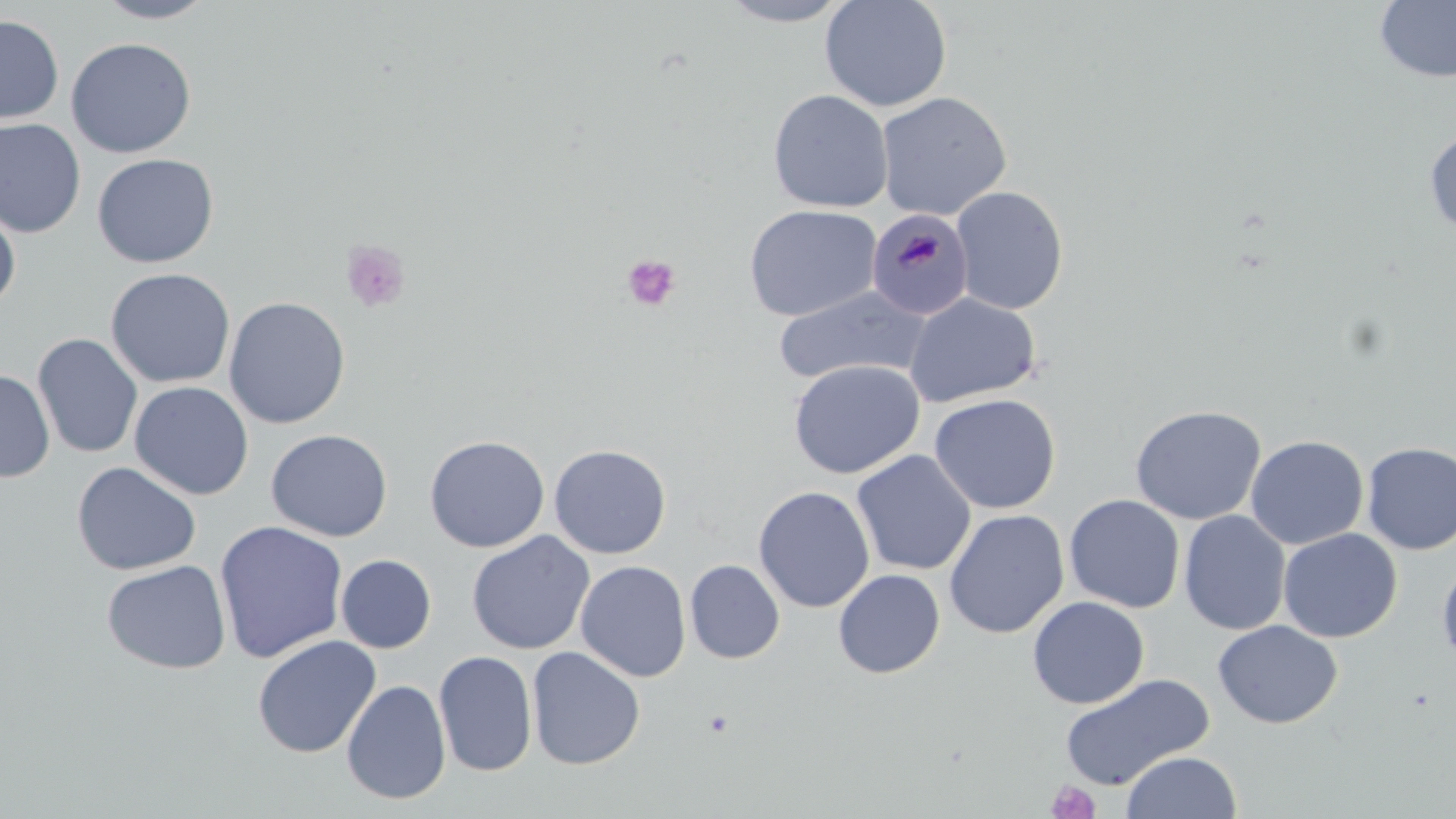

slide-level diagnosis = Plasmodium malariae
image size = 1456×819 pixels
uninfected red blood cell locations = approximate bounding boxes as [x1, y1, x2, y2] in pixels: [93, 0, 217, 24], [716, 0, 855, 26], [819, 0, 952, 113], [1374, 0, 1456, 84], [0, 14, 65, 125], [65, 37, 196, 158], [768, 89, 893, 212], [875, 91, 1012, 220], [0, 118, 86, 238], [1424, 127, 1456, 238], [91, 153, 219, 268], [950, 186, 1069, 314], [0, 202, 21, 311], [744, 204, 882, 322], [105, 268, 236, 389], [773, 285, 931, 386], [904, 293, 1041, 409], [223, 296, 351, 429], [32, 333, 143, 458], [788, 360, 925, 479], [0, 370, 55, 483], [129, 381, 254, 501], [929, 393, 1062, 514], [1129, 404, 1266, 525], [266, 429, 392, 542], [424, 435, 550, 553], [1245, 435, 1369, 550], [1361, 442, 1456, 555], [549, 443, 671, 559], [851, 450, 976, 576], [71, 462, 201, 576], [753, 486, 875, 613], [1064, 494, 1184, 613], [943, 509, 1069, 638], [1179, 511, 1291, 635], [214, 520, 348, 664], [1278, 528, 1402, 643], [467, 531, 594, 655], [336, 554, 436, 653], [1437, 558, 1456, 670], [101, 559, 231, 674], [684, 559, 785, 664], [575, 560, 691, 682], [833, 569, 945, 678], [1027, 597, 1150, 708], [1213, 620, 1343, 728], [252, 635, 381, 758], [527, 647, 646, 770], [433, 651, 538, 777], [1058, 673, 1215, 790], [341, 680, 452, 805], [1121, 751, 1242, 818]
preparation = thin blood smear
magnification = 1000x
Plasmodium malariae-infected red blood cell locations = approximate bounding boxes as [x1, y1, x2, y2] in pixels: [866, 208, 975, 321]
modality = light microscopy
stain = May-Grünwald-Giemsa
field of view = single
platelet locations = approximate bounding boxes as [x1, y1, x2, y2] in pixels: [339, 239, 411, 314], [621, 253, 680, 312], [1046, 780, 1101, 819]